Assess for malaria.
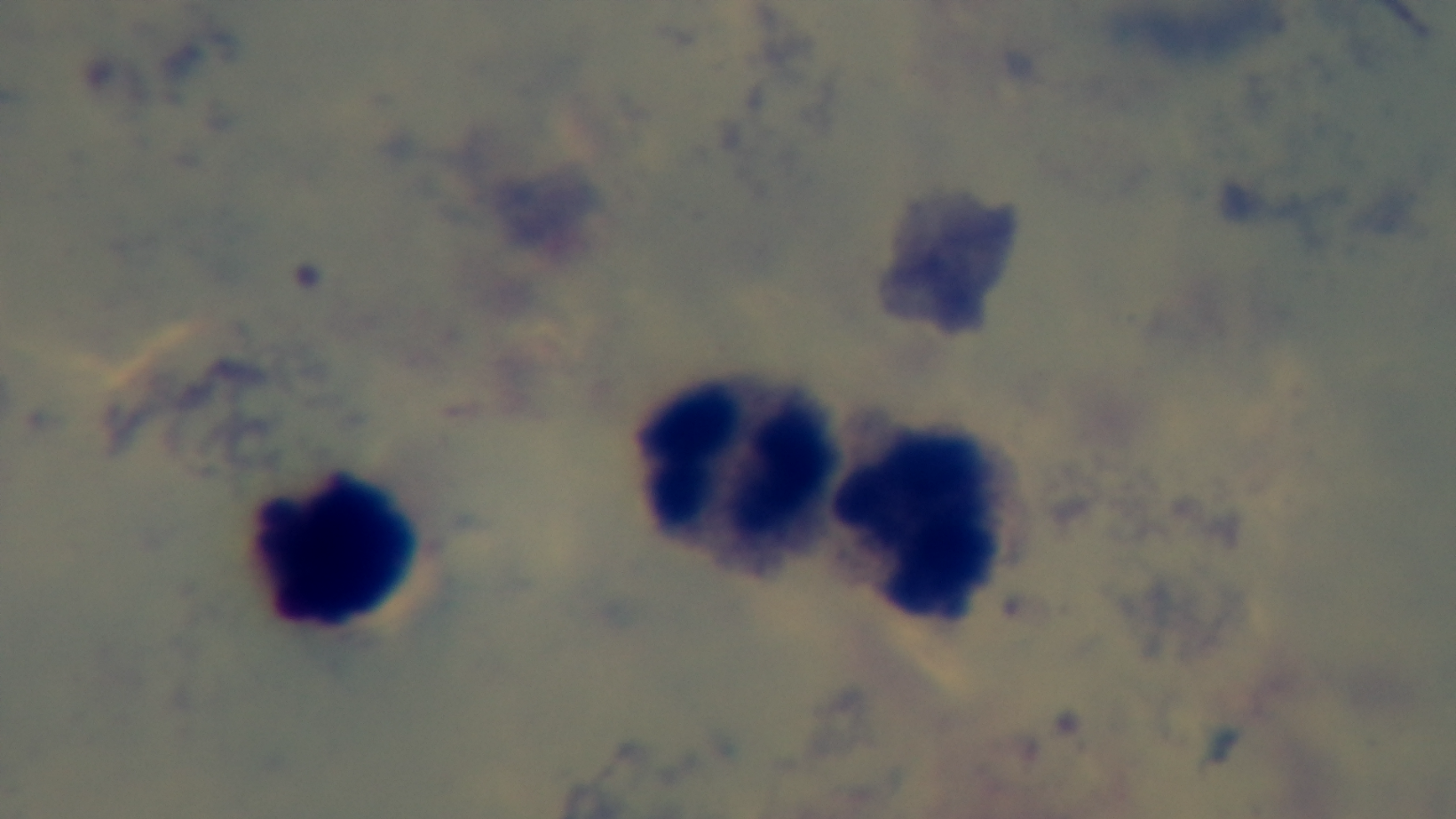
Negative.

Preparation: thick. One field from the slide. Mounted 4K digital camera. Giemsa stain. Oil-immersion objective, 100x. Light microscopy.